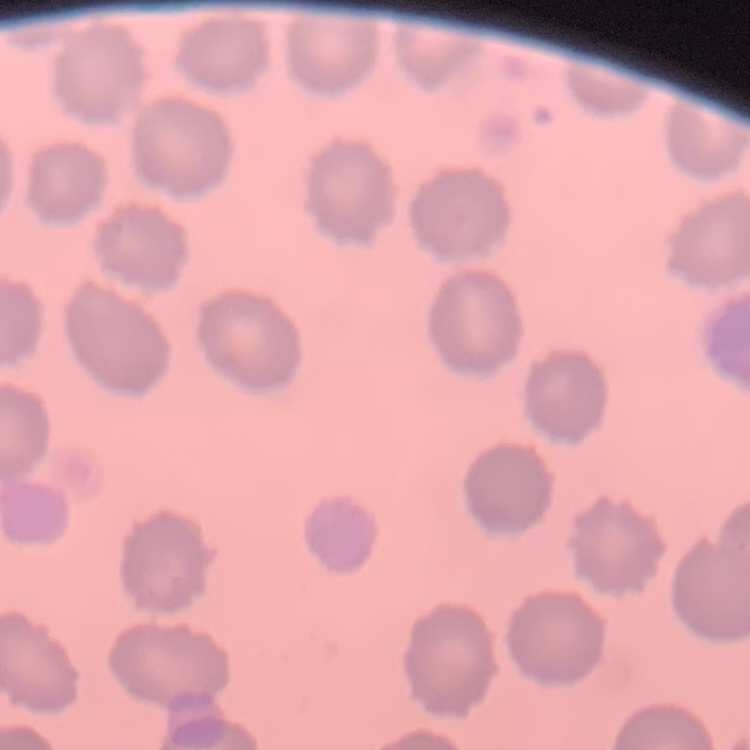

Summary:
  - Erythrocyte morphology: no rouleaux formation
  - Preparation: thin peripheral smear
  - Image type: square crop of a larger photomicrograph
  - Stain: Field's or Giemsa